Classify this cell by malaria status.
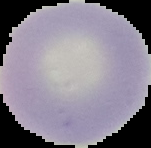
Uninfected.

image size = 151×148 pixels
image type = segmented cell region on a black background
preparation = thin blood film